State which parasite is depicted.
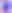
This is Toxoplasma gondii.

{
  "modality": "micrograph",
  "magnification": "400x"
}